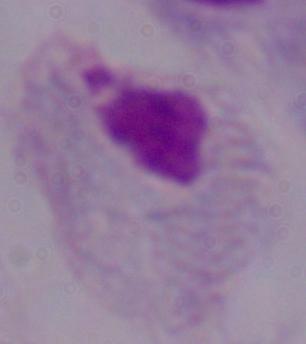
identification = trichomonad
modality = micrograph
magnification = 1000x